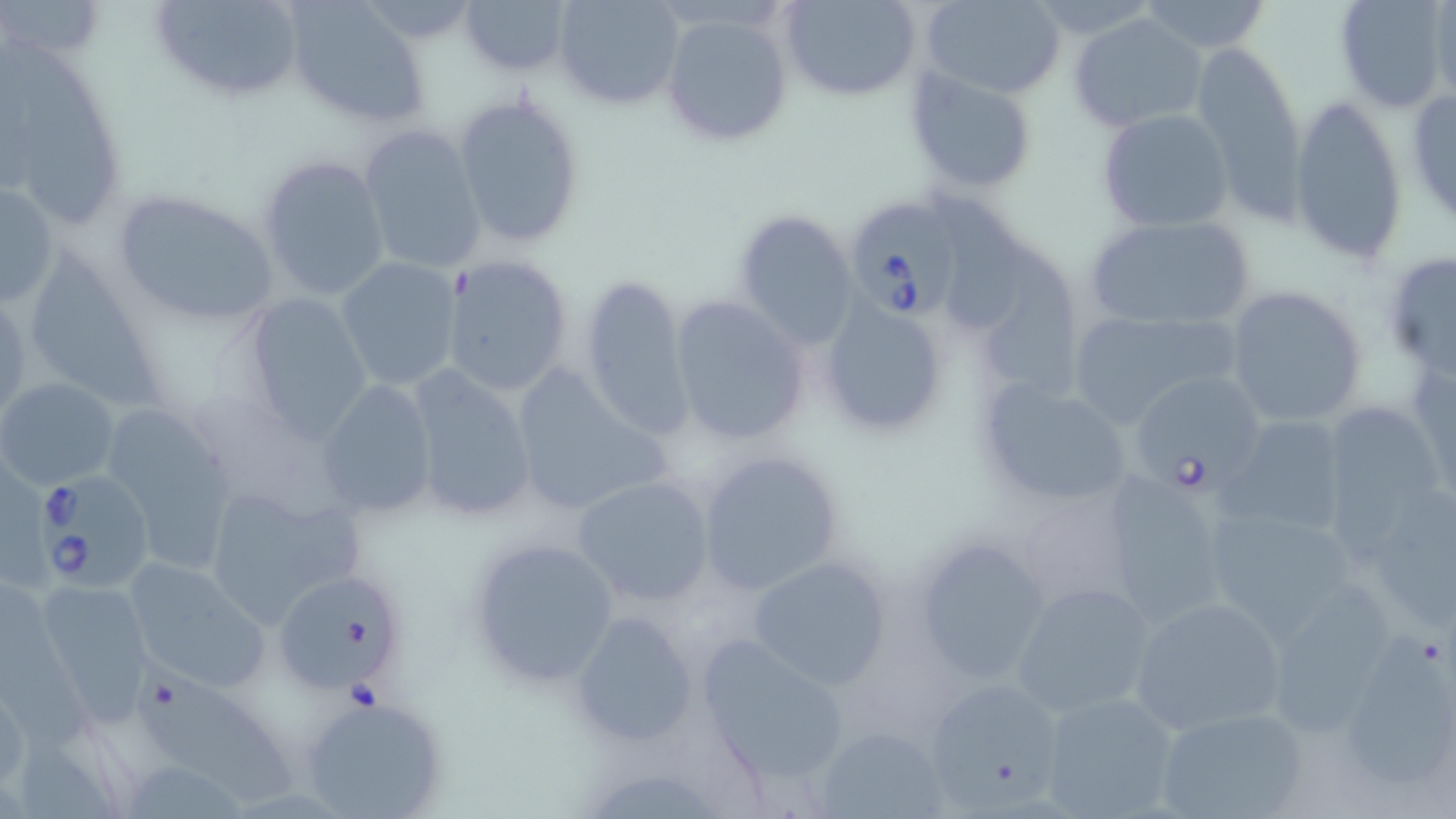

slide-level diagnosis = Babesia divergens
preparation = thin blood film
uninfected red blood cell locations = approximate bounding boxes as named x1/y1/x2/y2 corners in pixels: (x1=3, y1=0, x2=109, y2=63), (x1=147, y1=0, x2=309, y2=107), (x1=459, y1=0, x2=572, y2=78), (x1=782, y1=0, x2=923, y2=100), (x1=921, y1=0, x2=1069, y2=98), (x1=1333, y1=0, x2=1450, y2=115), (x1=553, y1=1, x2=686, y2=109), (x1=1139, y1=1, x2=1272, y2=53), (x1=1427, y1=2, x2=1456, y2=105), (x1=284, y1=3, x2=431, y2=130), (x1=661, y1=11, x2=796, y2=150), (x1=1068, y1=12, x2=1209, y2=133), (x1=0, y1=39, x2=127, y2=227), (x1=1192, y1=40, x2=1305, y2=206), (x1=904, y1=66, x2=1039, y2=198), (x1=451, y1=89, x2=589, y2=249), (x1=1404, y1=89, x2=1456, y2=228), (x1=1290, y1=95, x2=1407, y2=269), (x1=1097, y1=107, x2=1234, y2=233), (x1=357, y1=124, x2=486, y2=276), (x1=256, y1=154, x2=392, y2=301), (x1=132, y1=174, x2=402, y2=314), (x1=0, y1=177, x2=61, y2=311), (x1=931, y1=181, x2=1029, y2=334), (x1=108, y1=189, x2=282, y2=330), (x1=730, y1=209, x2=860, y2=349), (x1=1084, y1=213, x2=1257, y2=332), (x1=989, y1=232, x2=1091, y2=408), (x1=30, y1=239, x2=171, y2=415), (x1=1383, y1=251, x2=1456, y2=380), (x1=442, y1=255, x2=575, y2=399), (x1=334, y1=256, x2=462, y2=392), (x1=577, y1=272, x2=694, y2=441), (x1=1224, y1=284, x2=1370, y2=428), (x1=238, y1=293, x2=374, y2=443), (x1=666, y1=294, x2=811, y2=447), (x1=817, y1=301, x2=950, y2=435), (x1=1063, y1=309, x2=1237, y2=429), (x1=1410, y1=357, x2=1456, y2=503), (x1=507, y1=364, x2=671, y2=518), (x1=402, y1=366, x2=538, y2=525), (x1=1125, y1=373, x2=1264, y2=493), (x1=0, y1=377, x2=121, y2=490), (x1=317, y1=379, x2=438, y2=521), (x1=975, y1=379, x2=1133, y2=510), (x1=1317, y1=399, x2=1451, y2=545), (x1=108, y1=415, x2=238, y2=577), (x1=1220, y1=415, x2=1354, y2=537), (x1=695, y1=448, x2=847, y2=595), (x1=1093, y1=470, x2=1235, y2=628), (x1=572, y1=475, x2=715, y2=607), (x1=201, y1=482, x2=367, y2=628), (x1=1350, y1=484, x2=1456, y2=634), (x1=1009, y1=492, x2=1139, y2=611), (x1=1196, y1=501, x2=1360, y2=637), (x1=910, y1=534, x2=1052, y2=688), (x1=465, y1=535, x2=621, y2=691), (x1=747, y1=555, x2=894, y2=688), (x1=121, y1=558, x2=272, y2=694), (x1=279, y1=569, x2=406, y2=691), (x1=32, y1=580, x2=157, y2=722), (x1=1010, y1=581, x2=1157, y2=719), (x1=1258, y1=584, x2=1407, y2=741), (x1=1127, y1=594, x2=1290, y2=738), (x1=569, y1=611, x2=701, y2=749), (x1=696, y1=631, x2=854, y2=787), (x1=1339, y1=632, x2=1455, y2=791), (x1=137, y1=666, x2=301, y2=807), (x1=921, y1=676, x2=1066, y2=812), (x1=0, y1=681, x2=27, y2=788), (x1=1041, y1=690, x2=1183, y2=818), (x1=299, y1=694, x2=448, y2=819), (x1=1155, y1=703, x2=1307, y2=819), (x1=815, y1=725, x2=951, y2=817)
magnification = 1000x
stain = May-Grünwald-Giemsa
field of view = one of a larger specimen
modality = optical microscopy
Babesia divergens-infected red blood cell locations = approximate bounding boxes as named x1/y1/x2/y2 corners in pixels: (x1=841, y1=196, x2=974, y2=325), (x1=34, y1=473, x2=159, y2=593)
image size = 1456×819 pixels